Give a bounding box for every Plasmodium parasite.
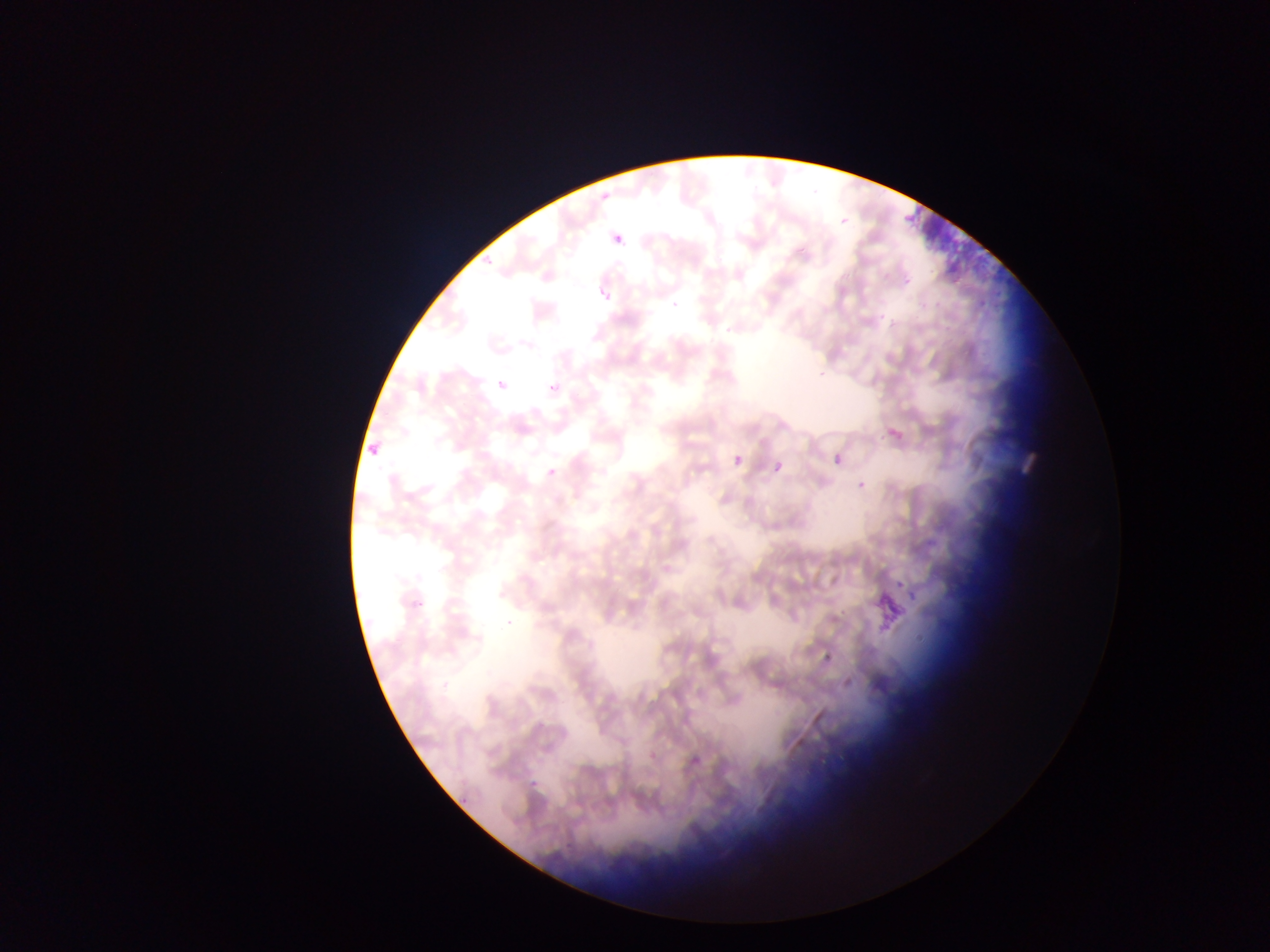

Approximate bounding boxes as left top right bottom in pixels.
Plasmodium parasites: 600 179 621 201; 839 211 854 225; 610 235 622 252; 481 257 491 269; 900 272 917 286; 599 289 617 302; 492 377 509 391; 546 381 558 392; 887 427 903 442; 832 448 846 463; 733 454 744 467; 543 458 561 476; 774 462 784 473; 853 480 864 492; 894 573 904 587; 904 581 921 602; 412 596 423 611; 528 779 535 789; 458 800 469 808.

image size = 1270×952 pixels
preparation = thin blood smear
field of view = single
country = Ghana
capture = mobile-phone photograph through a microscope